Classify this cell by malaria status.
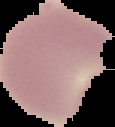
Uninfected.

image size = 115×127 pixels
image type = cell region segmented out of the field of view; surrounding area masked to black
preparation = thin blood film